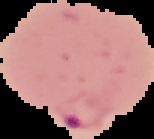
Summary:
  - Preparation: thin blood film
  - Result: Plasmodium parasites detected
  - Image size: 154×139 pixels
  - Image type: cell region segmented out of the field of view; surrounding area masked to black